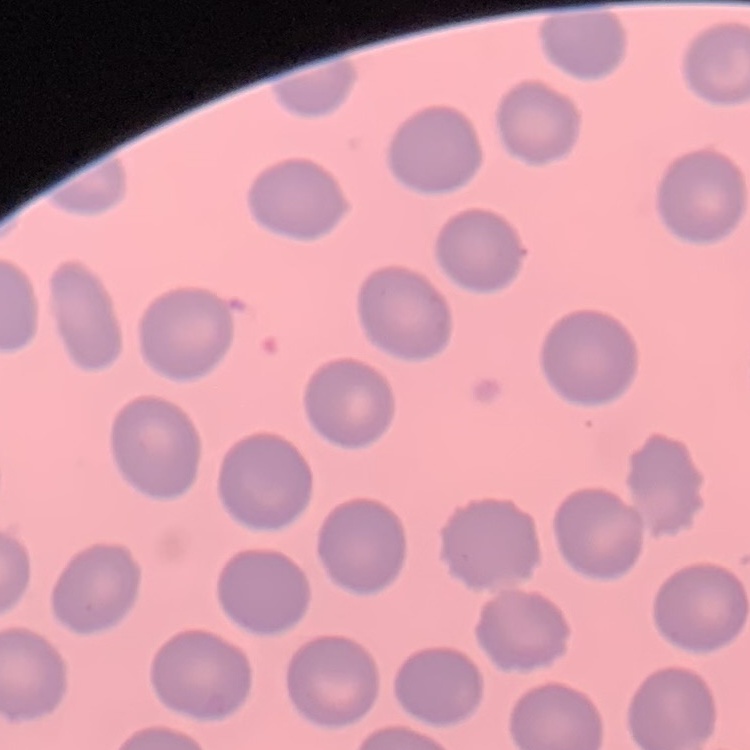
The erythrocytes show no rouleaux formation. Field's or Giemsa stain. Square crop of a larger photomicrograph. Thin blood smear.